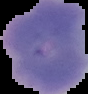 The area outside the segmented cell region is set to black. Image is 88×94 pixels. From a thin blood film. Malaria status: uninfected.